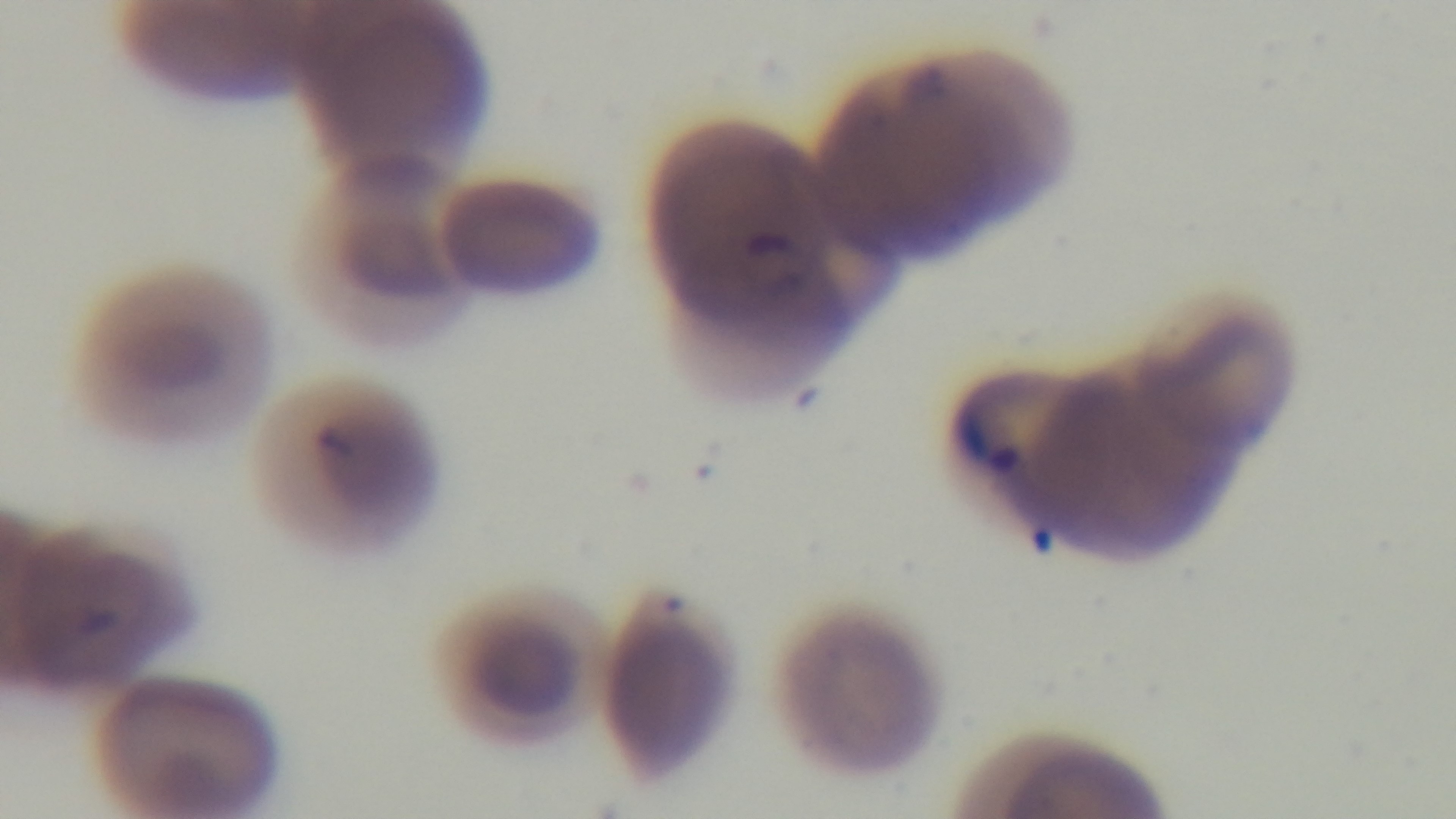

objective = 100x oil immersion
preparation = thin smear
field of view = one from the slide
stain = Giemsa
capture = mounted 4K digital camera
malaria status = infected
modality = light microscopy